Describe the morphology of the erythrocytes.
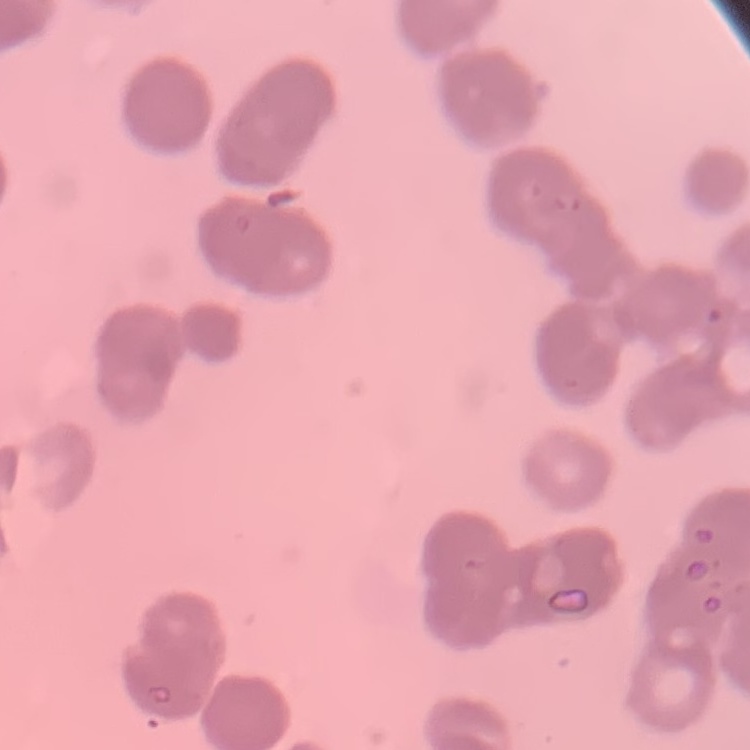
They show rouleaux formation.

Summary:
  - Preparation: thin blood film
  - Stain: Field's or Giemsa
  - Image type: one tile cut from a larger photomicrograph